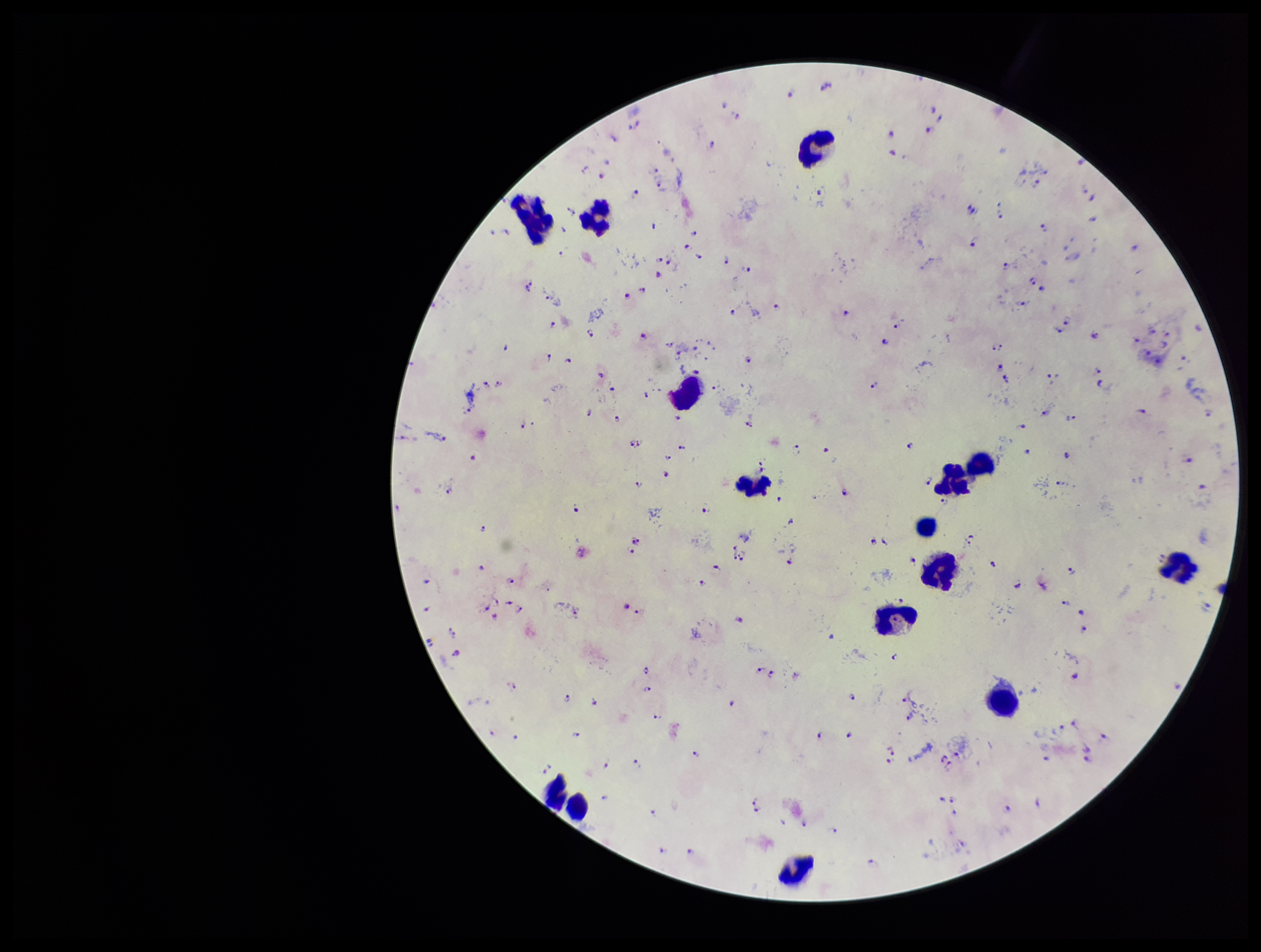

Summary:
  - Capture: smartphone photograph through the microscope eyepiece
  - Leukocyte count: 14
  - Plasmodium parasites: detected
  - Stain: Giemsa
  - Patient malaria status: infected
  - Field of view: one from this slide
  - Preparation: thick
  - Species reported for this patient: Plasmodium falciparum
  - Image size: 1261×952 pixels
  - Parasite count: 141